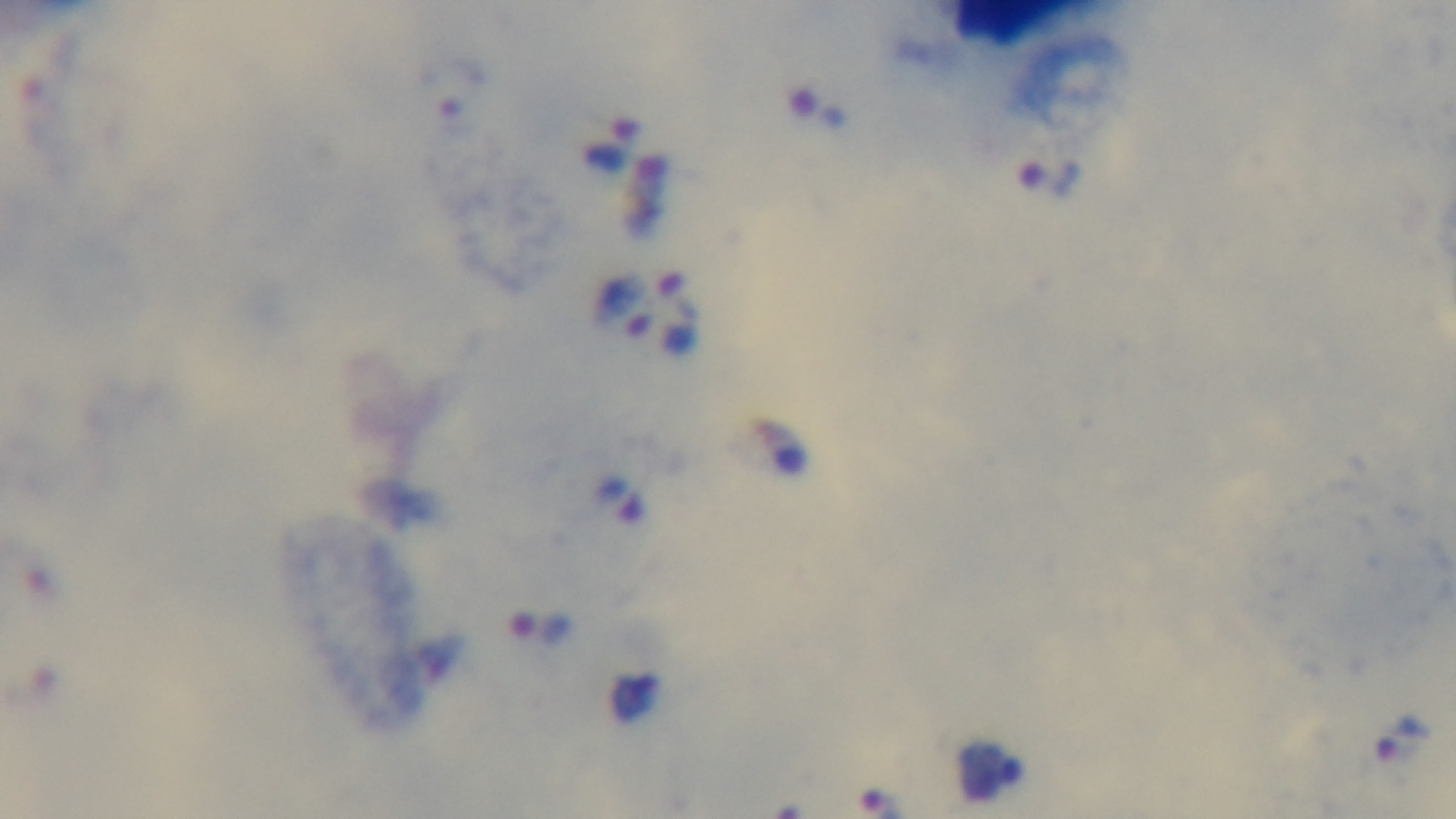

Summary:
  - Objective: 100x oil immersion
  - Capture: mounted 4K digital camera
  - Modality: light microscopy
  - Malaria status: infected
  - Field of view: single
  - Stain: Giemsa
  - Preparation: thick smear